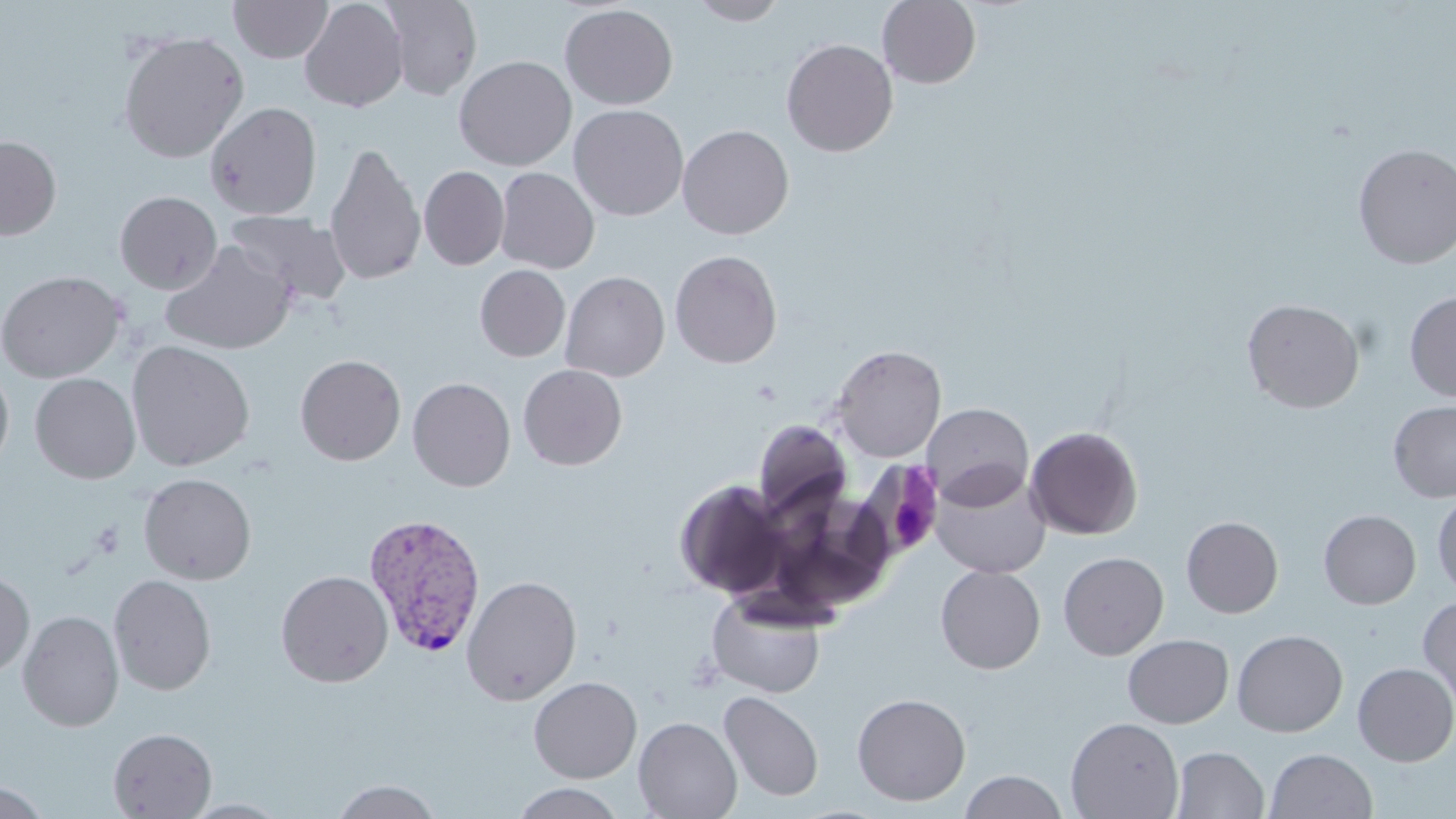
Summary:
  - Coordinate format: approximate bounding boxes as (x1, y1, x2, y2) in pixels
  - Plasmodium vivax-infected red blood cell locations: (362, 512, 486, 658)
  - Uninfected red blood cell locations: (229, 0, 333, 63), (299, 0, 408, 113), (381, 0, 482, 100), (877, 0, 981, 89), (687, 1, 790, 25), (559, 4, 678, 110), (116, 30, 250, 164), (781, 38, 898, 157), (453, 55, 577, 171), (205, 101, 322, 220), (569, 104, 688, 221), (677, 124, 794, 239), (0, 136, 61, 240), (324, 142, 426, 286), (1352, 143, 1456, 270), (419, 165, 509, 271), (495, 167, 599, 274), (114, 190, 222, 294), (226, 209, 350, 304), (161, 242, 295, 355), (669, 250, 782, 368), (474, 264, 570, 362), (0, 270, 125, 383), (560, 271, 670, 382), (1404, 291, 1456, 402), (1242, 298, 1365, 414), (127, 340, 255, 472), (831, 345, 946, 462), (295, 354, 406, 465), (0, 363, 15, 479), (518, 364, 627, 470), (30, 372, 141, 484), (407, 377, 516, 491), (1388, 399, 1456, 504), (921, 403, 1033, 509), (753, 420, 852, 520), (1025, 426, 1143, 540), (930, 465, 1051, 579), (138, 472, 257, 585), (674, 479, 792, 599), (1432, 493, 1456, 601), (1318, 509, 1421, 609), (1181, 516, 1283, 618), (1058, 551, 1168, 660), (935, 565, 1046, 674), (0, 570, 35, 678), (276, 570, 393, 687), (109, 574, 216, 695), (461, 575, 582, 706), (707, 592, 827, 698), (1418, 596, 1456, 709), (18, 610, 124, 732), (1232, 629, 1348, 737), (1123, 634, 1234, 728), (1352, 662, 1456, 766), (529, 676, 642, 783), (719, 690, 824, 802), (852, 692, 971, 806), (633, 716, 742, 819), (1065, 716, 1184, 819), (108, 727, 217, 818), (1170, 746, 1269, 819), (1265, 748, 1378, 819), (959, 770, 1068, 818), (0, 779, 52, 818), (329, 779, 443, 819), (509, 783, 628, 819), (179, 799, 293, 818)
  - Slide-level diagnosis: Plasmodium vivax
  - Modality: light microscopy
  - Magnification: 1000x
  - Field of view: one of a larger specimen
  - Preparation: thin blood film
  - Stain: May-Grünwald-Giemsa
  - Image size: 1456×819 pixels